Classify this cell by malaria status.
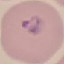
Parasitized.

Thin blood film. Giemsa stain. Cell patch, automatically extracted from a larger field of view and resized to 64 × 64 pixels. Photographed with a smartphone camera at the microscope eyepiece.